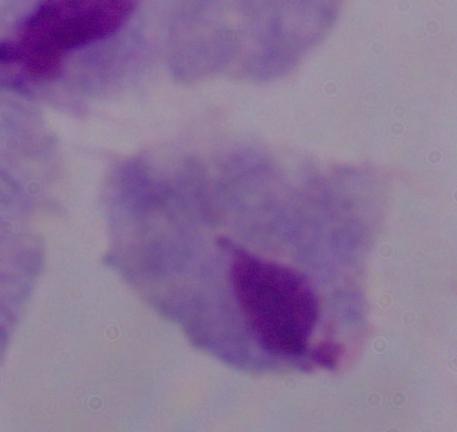
Summary:
  - Modality: photomicrograph
  - Magnification: 1000x
  - Identification: trichomonad